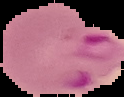
Segmented cell region on a black background. From a thin blood smear. Result: malaria parasites identified. Image is 124×97 pixels.